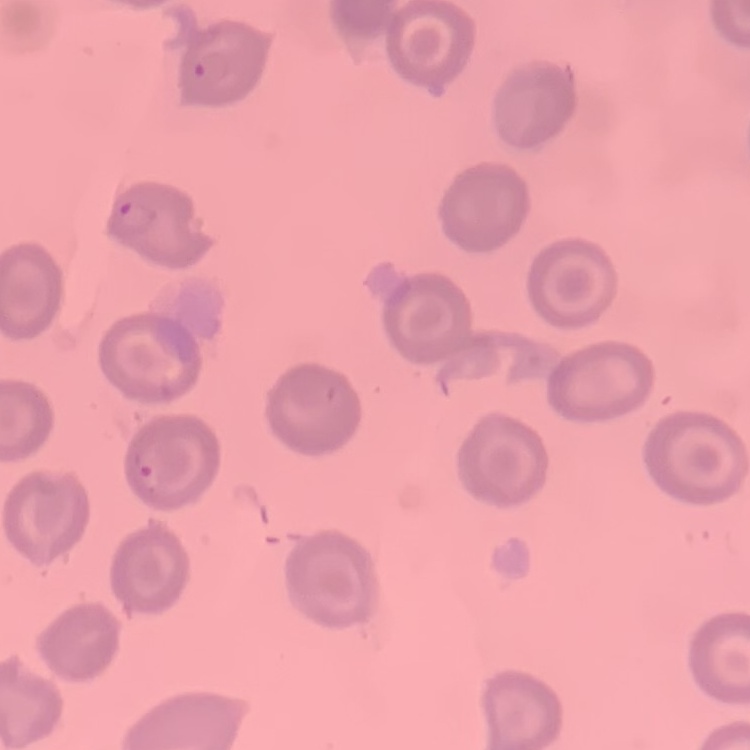
Summary:
  - Erythrocyte morphology: no rouleaux formation
  - Preparation: thin blood film
  - Stain: Field's or Giemsa
  - Image type: one tile cut from a larger photomicrograph